Assess this cell for malaria.
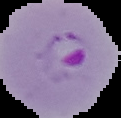

Parasitized.

The area outside the segmented cell region is set to black. From a thin blood smear. Image is 121×118 pixels.